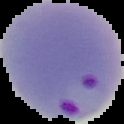 Cell region segmented out of the field of view; the surrounding area is masked to black. Malaria status: parasitized. Image is 124×124 pixels. From a thin blood film.